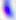

Summary:
  - Modality: photomicrograph
  - Identification: Toxoplasma gondii
  - Magnification: 400x